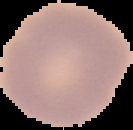
image size = 133×130 pixels
preparation = thin blood smear
malaria status = uninfected
image type = segmented cell region with the area outside set to black